Classify this cell by malaria status.
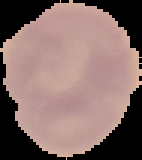

It is uninfected.

Summary:
  - Image type: segmented cell region on a black background
  - Image size: 142×160 pixels
  - Preparation: thin blood smear